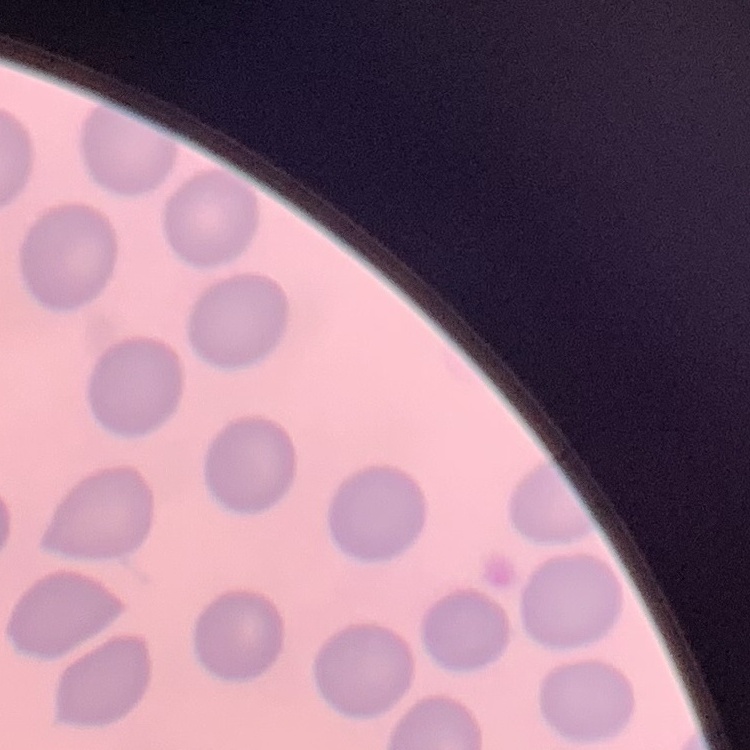

erythrocyte_morphology: no rouleaux formation
image_type: one tile cut from a larger photomicrograph
preparation: thin blood smear
stain: Field's or Giemsa